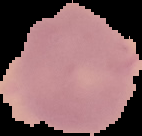

{
  "image_type": "cell region segmented out of the field of view; surrounding area masked to black",
  "preparation": "thin blood smear",
  "malaria_status": "uninfected",
  "image_size": "142×136 pixels"
}